Comment on the morphology of the red blood cells.
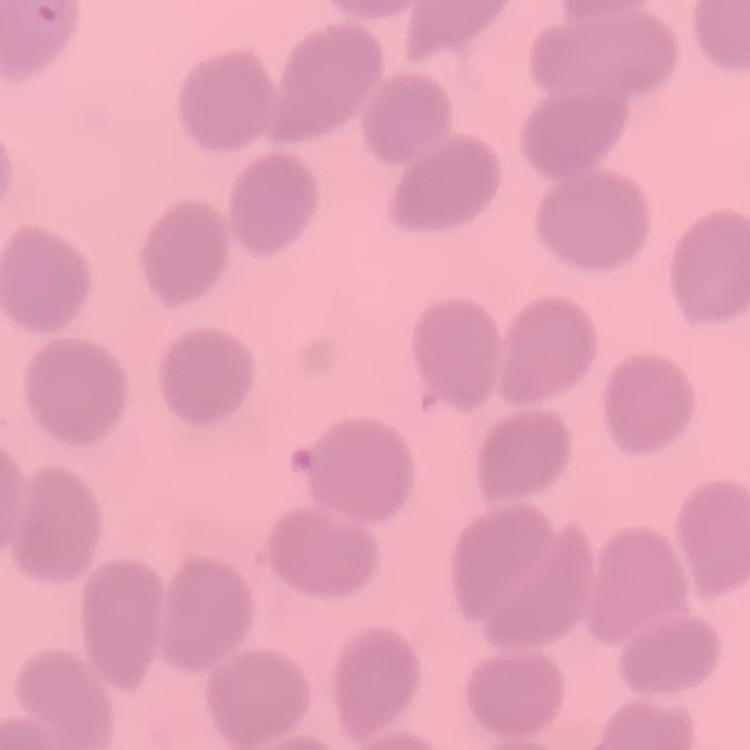

No rouleaux formation.

Thin peripheral smear. Field's or Giemsa stain. Square crop of a larger photomicrograph.